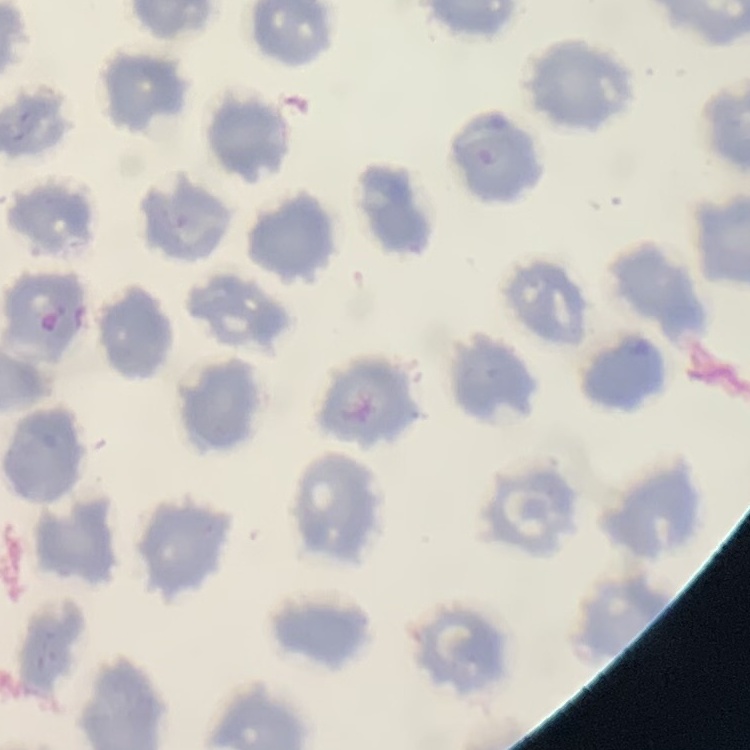
Summary:
  - Erythrocyte morphology: no rouleaux formation
  - Stain: Field's or Giemsa
  - Image type: square crop of a larger photomicrograph
  - Preparation: thin blood smear